Evaluate for malaria.
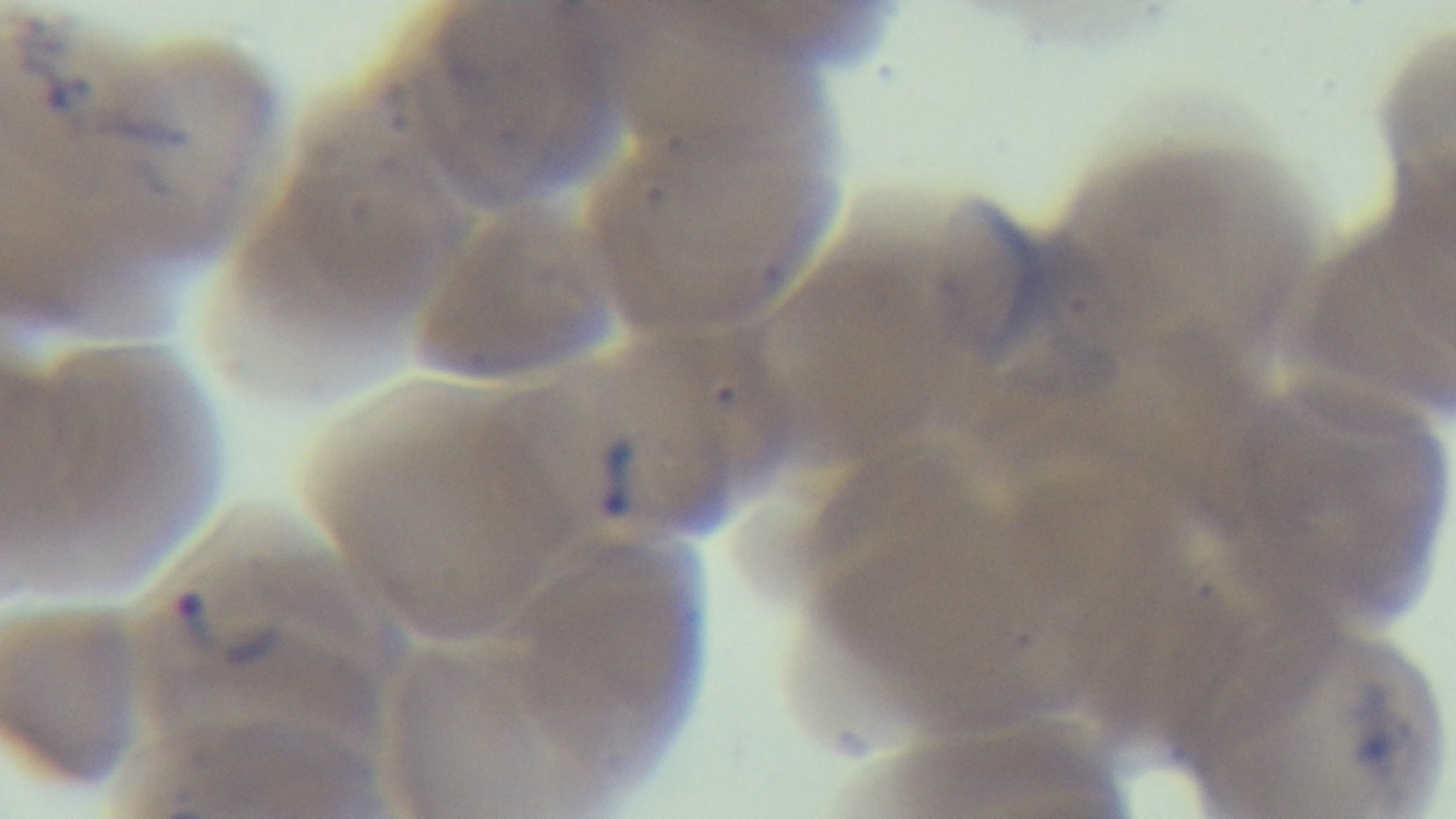
It is infected.

Single field of view. Light microscopy. Giemsa stain. Oil-immersion objective, 100x. Preparation: thin. Captured with a mounted 4K digital camera.